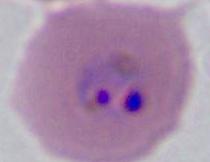
modality: photomicrograph
identification: Plasmodium
magnification: 400x or 1000x